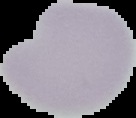

From a thin blood film. Malaria status: uninfected. The area outside the segmented cell region is set to black. Image is 136×118 pixels.